Locate every blood parasite and identify its species.
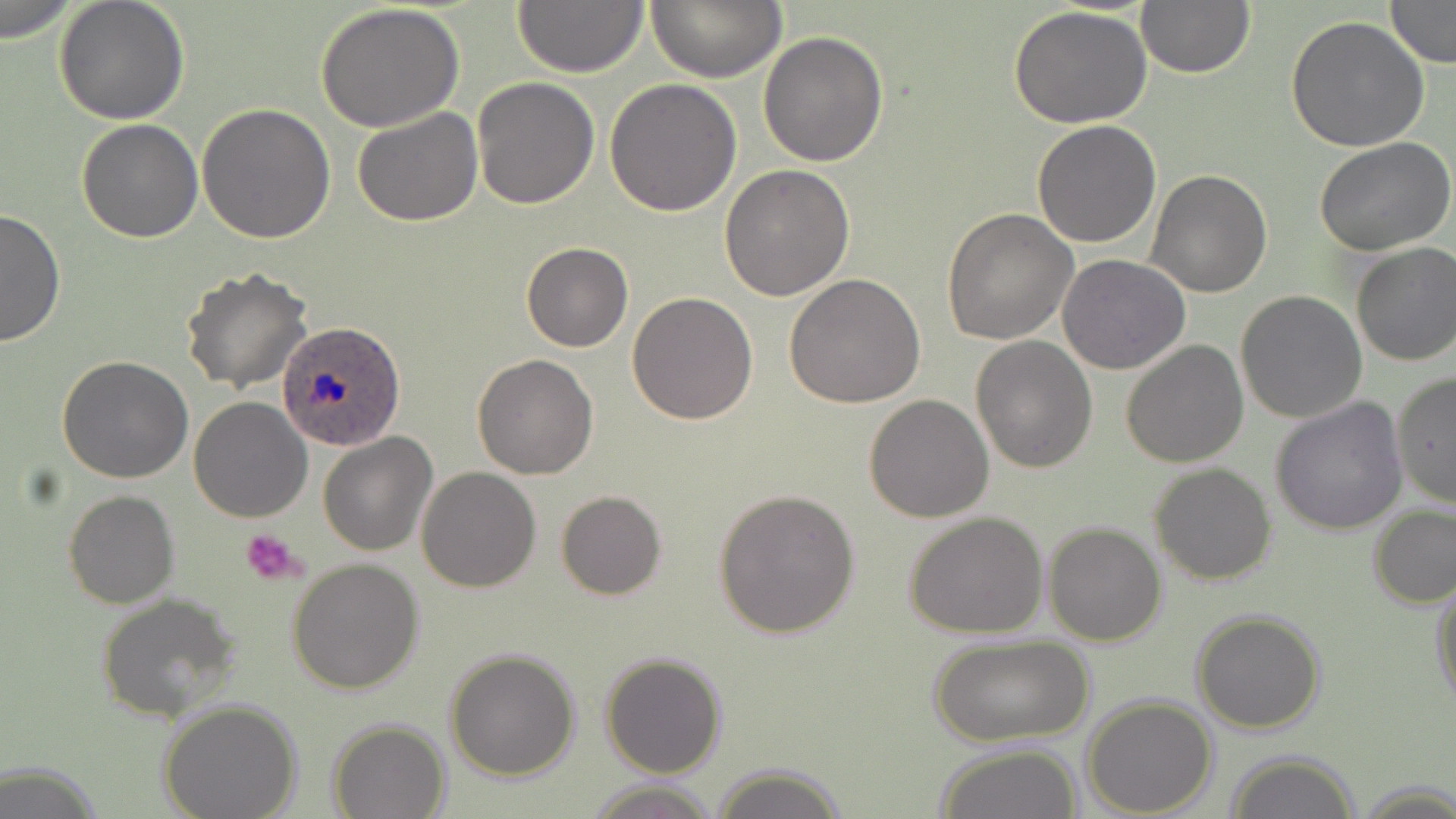
Approximate bounding boxes as (x1,y1)-(x2,y2) corner pairs in pixels.
Plasmodium ovale-infected red blood cells: (278,322)-(405,449).
No Plasmodium falciparum, Plasmodium malariae, Plasmodium vivax, Babesia divergens, or Trypanosoma brucei observed.

Uninfected red blood cell locations: (2,0)-(76,46), (52,0)-(189,124), (646,0)-(787,83), (1135,0)-(1256,79), (1383,0)-(1455,67), (511,1)-(648,77), (317,4)-(466,133), (1008,7)-(1154,130), (1285,16)-(1431,153), (758,30)-(888,168), (473,77)-(601,210), (604,77)-(743,216), (357,95)-(597,218), (197,102)-(336,244), (351,106)-(483,227), (76,119)-(204,242), (1031,120)-(1163,249), (1313,137)-(1456,258), (720,165)-(857,302), (1147,170)-(1272,297), (0,208)-(65,346), (941,209)-(1078,344), (520,241)-(633,352), (1351,242)-(1456,368), (1057,255)-(1191,375), (180,266)-(314,392), (784,273)-(925,409), (1235,291)-(1367,425), (627,292)-(759,425), (969,334)-(1098,471), (1119,338)-(1250,467), (472,354)-(601,479), (58,355)-(192,483), (1392,373)-(1456,508), (864,393)-(994,522), (187,396)-(312,522), (1270,398)-(1408,537), (318,431)-(437,557), (1149,462)-(1276,586), (417,467)-(542,592), (713,487)-(860,638), (63,490)-(179,609), (555,490)-(667,600), (1368,505)-(1456,608), (903,512)-(1048,640), (1043,522)-(1167,646), (286,557)-(424,695), (1430,573)-(1456,709), (96,593)-(244,723), (1191,609)-(1327,734), (929,635)-(1091,749), (444,646)-(581,781), (599,652)-(727,777), (1081,694)-(1218,817), (158,699)-(302,819), (327,719)-(449,819), (933,741)-(1084,819), (1225,750)-(1363,819), (711,763)-(848,819), (582,779)-(723,817), (1358,781)-(1456,817). Platelet locations: (242,526)-(306,587). Slide-level diagnosis: Plasmodium ovale. One field of a larger specimen. Thin blood smear. Optical microscopy. Image is 1456×819 pixels. May-Grünwald-Giemsa-stained preparation. 1000x magnification.